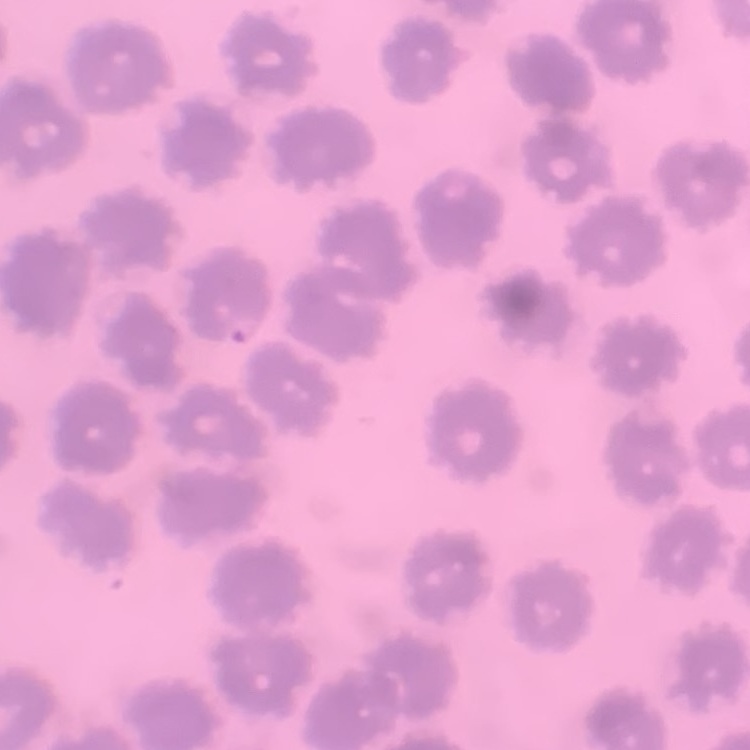

The red blood cells exhibit no rouleaux formation. Square crop of a larger photomicrograph. Stained with either Field's or Giemsa. Thin blood smear.